Outline each blood parasite and name the species.
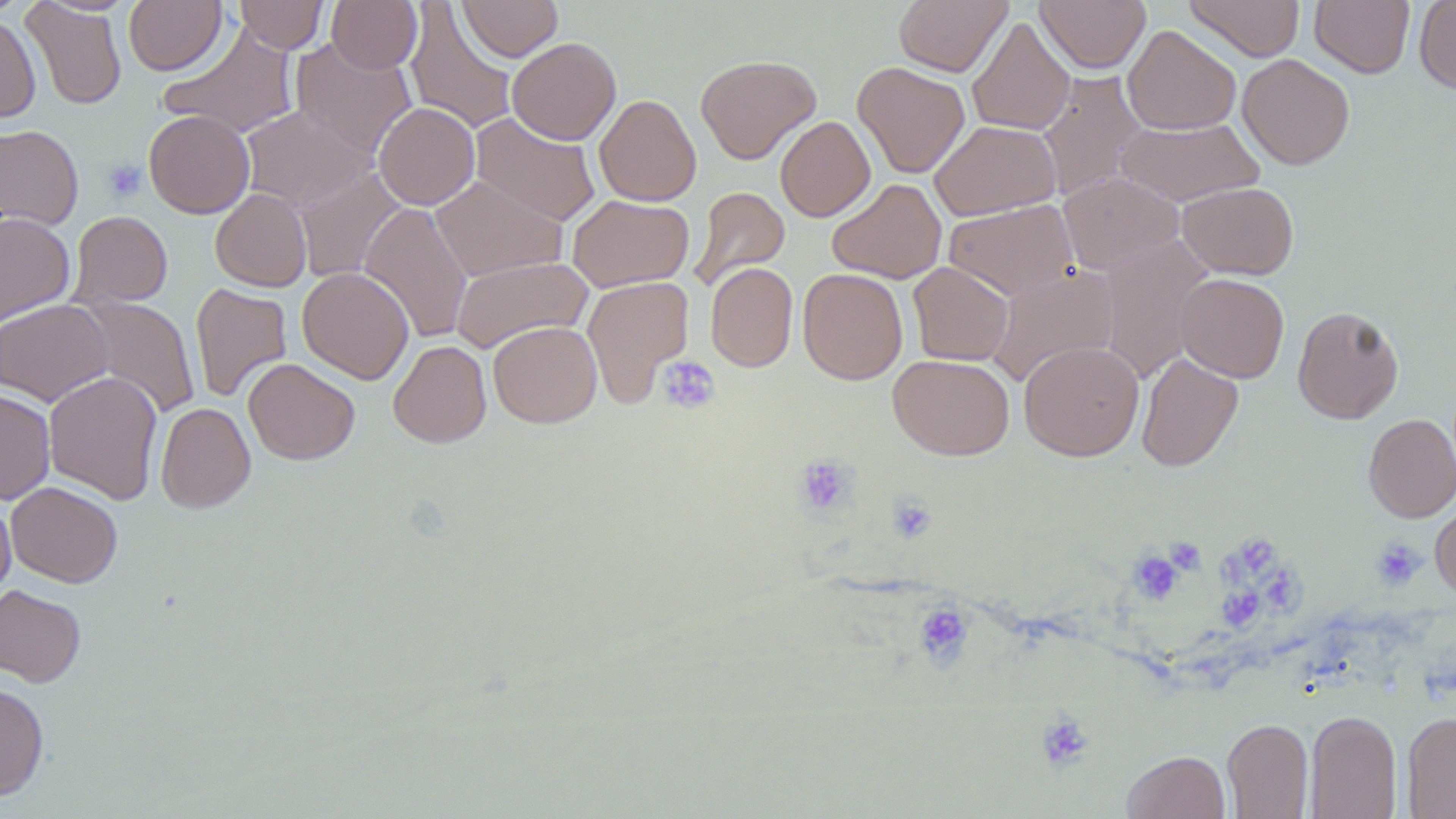

No blood parasites seen.

Summary:
  - Coordinate format: approximate bounding boxes as [x1, y1, x2, y2] in pixels
  - Uninfected red blood cell locations: [234, 0, 329, 53], [458, 0, 563, 62], [894, 0, 1012, 76], [1034, 0, 1150, 73], [1185, 0, 1305, 61], [1310, 0, 1414, 78], [1413, 0, 1456, 94], [22, 1, 127, 110], [123, 1, 227, 75], [326, 1, 422, 74], [405, 2, 518, 136], [0, 13, 41, 123], [966, 16, 1076, 136], [159, 24, 299, 139], [1122, 25, 1241, 135], [289, 37, 416, 159], [506, 37, 621, 145], [1237, 53, 1355, 169], [695, 54, 822, 165], [852, 61, 970, 178], [1036, 71, 1149, 201], [594, 94, 702, 207], [373, 102, 480, 209], [241, 105, 374, 213], [143, 110, 255, 218], [471, 113, 600, 227], [775, 116, 875, 222], [1114, 117, 1264, 206], [930, 120, 1061, 220], [0, 124, 84, 230], [294, 167, 406, 284], [1058, 172, 1183, 276], [429, 175, 567, 282], [827, 178, 947, 283], [1177, 182, 1298, 279], [689, 186, 790, 291], [210, 188, 312, 292], [568, 194, 694, 292], [943, 199, 1078, 301], [359, 202, 473, 344], [67, 210, 173, 309], [0, 213, 75, 325], [1096, 235, 1214, 381], [451, 255, 593, 353], [705, 262, 798, 372], [908, 262, 1014, 366], [986, 264, 1120, 388], [297, 267, 414, 384], [797, 268, 908, 384], [1175, 273, 1289, 383], [582, 276, 694, 407], [190, 283, 292, 403], [76, 295, 201, 419], [0, 299, 113, 406], [1292, 305, 1404, 424], [488, 320, 602, 427], [389, 340, 491, 448], [1018, 340, 1144, 461], [1136, 351, 1243, 472], [888, 354, 1014, 460], [243, 358, 360, 465], [44, 371, 163, 504], [0, 388, 56, 504], [155, 402, 255, 513], [1364, 414, 1456, 522], [6, 482, 123, 588], [0, 494, 15, 599], [1430, 500, 1456, 598], [0, 584, 86, 687], [0, 681, 49, 801], [1304, 710, 1401, 819], [1401, 711, 1456, 818], [1222, 718, 1313, 818], [1122, 750, 1230, 819]
  - Platelet locations: [102, 158, 147, 203], [657, 356, 721, 414], [794, 455, 858, 516], [886, 495, 938, 543], [1245, 535, 1282, 577], [1164, 536, 1206, 575], [1371, 537, 1426, 591], [1128, 550, 1184, 605], [1217, 550, 1251, 584], [1264, 573, 1309, 616], [1222, 581, 1268, 631], [914, 601, 973, 668], [1035, 712, 1095, 772]
  - Slide-level diagnosis: negative for blood parasites
  - Field of view: one of a larger specimen
  - Stain: May-Grünwald-Giemsa
  - Image size: 1456×819 pixels
  - Modality: optical microscopy
  - Magnification: 1000x
  - Preparation: thin blood film